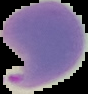

image size = 88×94 pixels
image type = segmented cell region with the area outside set to black
result = Plasmodium parasites detected
preparation = thin blood film